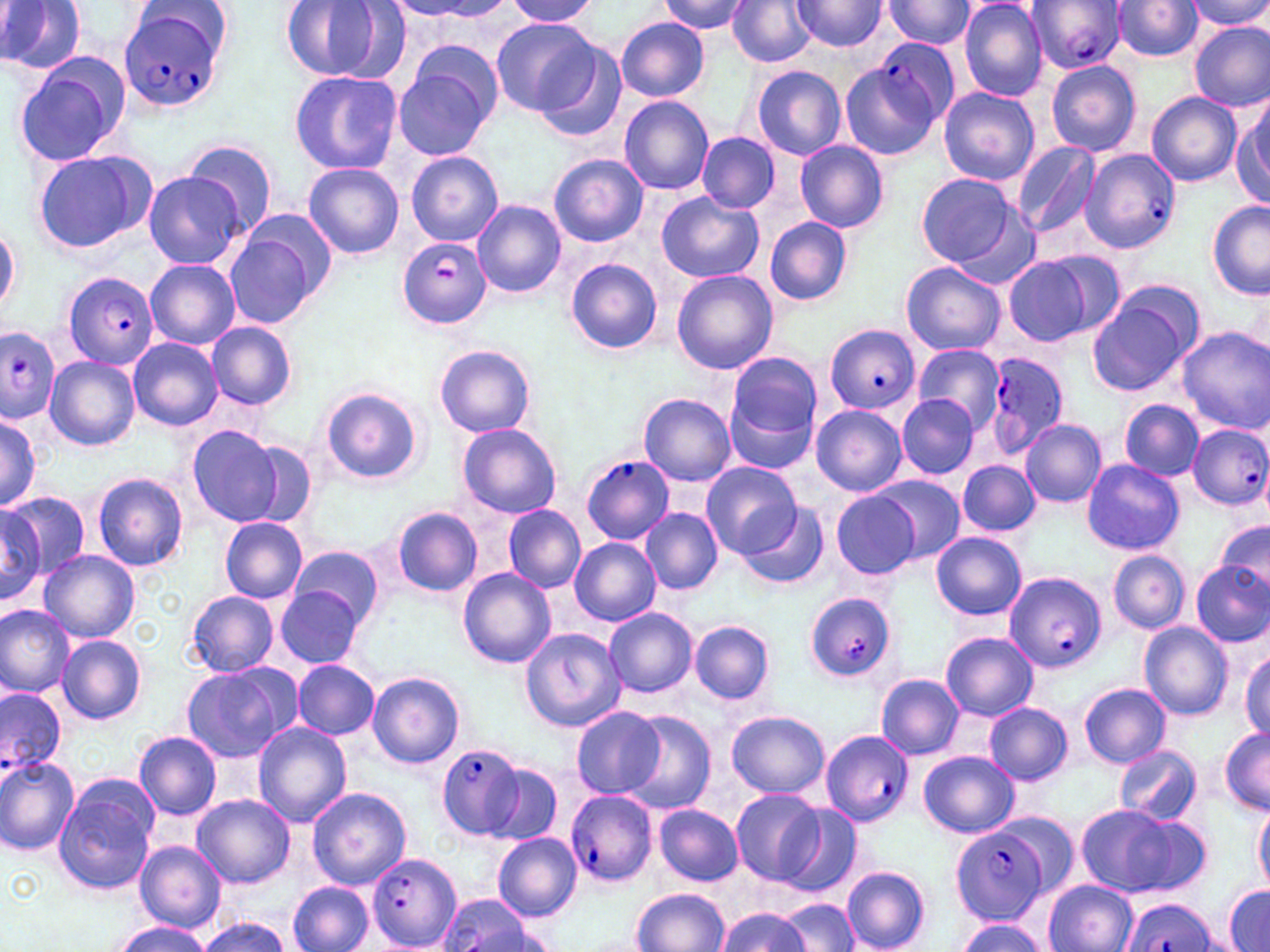
Summary:
  - Coordinate format: approximate bounding boxes as (x1,y1)-(x2,y2) corner pairs in pixels
  - Plasmodium falciparum-infected red blood cell locations: (1026,0)-(1126,73), (119,5)-(227,116), (876,40)-(957,126), (1080,148)-(1181,253), (397,237)-(490,327), (63,273)-(159,369), (824,323)-(919,414), (0,327)-(61,421), (982,350)-(1070,458), (1187,424)-(1270,510), (580,454)-(674,544), (1007,571)-(1106,674), (806,592)-(896,683), (0,688)-(66,778), (820,730)-(913,827), (437,743)-(525,838), (564,788)-(657,888), (948,825)-(1053,925), (368,853)-(462,950), (437,893)-(544,952), (1121,899)-(1217,952)
  - Uninfected red blood cell locations: (662,0)-(752,35), (727,0)-(813,67), (883,0)-(975,50), (959,0)-(1049,103), (1187,0)-(1270,30), (0,1)-(88,75), (278,1)-(388,84), (504,1)-(599,26), (789,1)-(889,53), (1111,1)-(1202,62), (491,17)-(601,117), (617,17)-(709,101), (1190,23)-(1268,111), (533,43)-(627,143), (12,54)-(129,168), (1046,60)-(1141,156), (392,62)-(496,161), (839,63)-(941,161), (750,65)-(847,161), (289,71)-(402,175), (938,88)-(1040,184), (1147,92)-(1240,185), (619,96)-(714,196), (1234,97)-(1270,208), (696,131)-(780,214), (184,139)-(278,236), (794,140)-(889,233), (1012,142)-(1100,241), (32,150)-(153,253), (406,152)-(504,245), (549,153)-(648,247), (303,163)-(404,260), (144,171)-(248,270), (917,173)-(1020,269), (656,191)-(765,283), (472,201)-(565,297), (1207,201)-(1270,296), (764,216)-(853,305), (0,224)-(21,315), (224,230)-(322,328), (1002,251)-(1117,346), (566,258)-(663,355), (145,259)-(240,350), (901,262)-(1005,356), (672,269)-(778,375), (1088,288)-(1199,396), (207,322)-(297,410), (1176,328)-(1269,432), (128,338)-(222,431), (434,345)-(538,438), (913,345)-(1006,430), (725,350)-(824,464), (45,356)-(139,451), (321,386)-(424,483), (638,394)-(736,486), (897,394)-(978,478), (1119,400)-(1203,481), (811,405)-(907,497), (0,415)-(42,512), (1021,420)-(1105,508), (456,422)-(562,519), (187,425)-(284,527), (243,440)-(320,530), (957,461)-(1040,535), (1082,461)-(1184,555), (701,462)-(800,560), (92,472)-(188,571), (871,474)-(964,564), (2,491)-(89,576), (832,491)-(920,577), (740,502)-(829,590), (0,504)-(46,607), (504,505)-(585,592), (390,506)-(483,597), (642,509)-(721,593), (220,516)-(308,604), (1213,518)-(1270,601), (931,532)-(1027,621), (570,538)-(660,625), (291,546)-(382,626), (38,549)-(139,643), (1108,549)-(1189,633), (1190,560)-(1269,647), (457,568)-(557,668), (275,587)-(363,667), (183,590)-(279,678), (0,606)-(74,699), (604,608)-(697,698), (689,620)-(775,705), (1138,622)-(1233,721), (519,625)-(626,732), (941,631)-(1037,721), (56,633)-(145,725), (1241,648)-(1270,740), (292,660)-(379,739), (181,663)-(298,763), (367,672)-(465,769), (876,673)-(965,760), (1079,683)-(1171,767), (983,702)-(1071,784), (570,708)-(666,798), (622,711)-(716,813), (727,711)-(830,798), (252,722)-(352,827), (1219,728)-(1269,814), (134,730)-(222,819), (1113,745)-(1200,825), (918,751)-(1019,838), (0,754)-(79,855), (0,761)-(155,868), (485,765)-(561,844), (55,782)-(157,893), (307,787)-(411,889), (729,788)-(824,883), (192,793)-(296,888), (1253,798)-(1270,893), (777,803)-(861,897), (654,804)-(742,886), (1074,804)-(1195,897), (492,833)-(582,921), (134,841)-(227,932), (841,866)-(931,952), (1043,880)-(1138,952), (287,881)-(373,952), (1224,885)-(1269,952), (631,888)-(730,952), (781,899)-(859,951), (717,907)-(812,952), (197,917)-(293,952), (956,918)-(1051,952), (115,921)-(214,951)
  - Slide-level diagnosis: Plasmodium falciparum
  - Image size: 1270×952 pixels
  - Magnification: 1000x
  - Stain: May-Grünwald-Giemsa
  - Field of view: one of a larger specimen
  - Preparation: thin blood smear
  - Modality: optical microscopy